Report the malaria status of this cell.
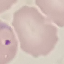

Parasitized.

stain = Giemsa
preparation = thin blood smear
capture = smartphone camera at the microscope eyepiece
image type = cell patch, automatically extracted from a larger field of view and resized to 64 × 64 pixels